Classify this cell by malaria status.
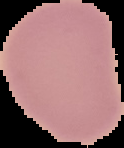

Uninfected.

{
  "preparation": "thin blood smear",
  "image_type": "cell region segmented out of the field of view; surrounding area masked to black",
  "image_size": "124×148 pixels"
}